State which cell type is depicted.
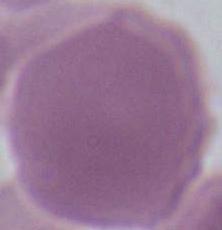
This is an erythrocyte.

Summary:
  - Modality: photomicrograph
  - Magnification: 1000x